Name the parasite shown.
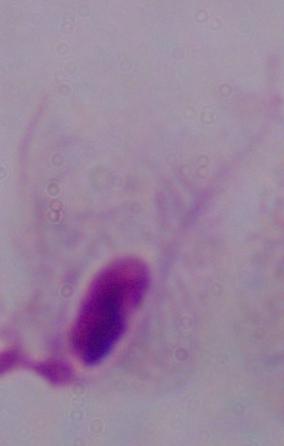

A trichomonad.

Summary:
  - Modality: micrograph
  - Magnification: 1000x